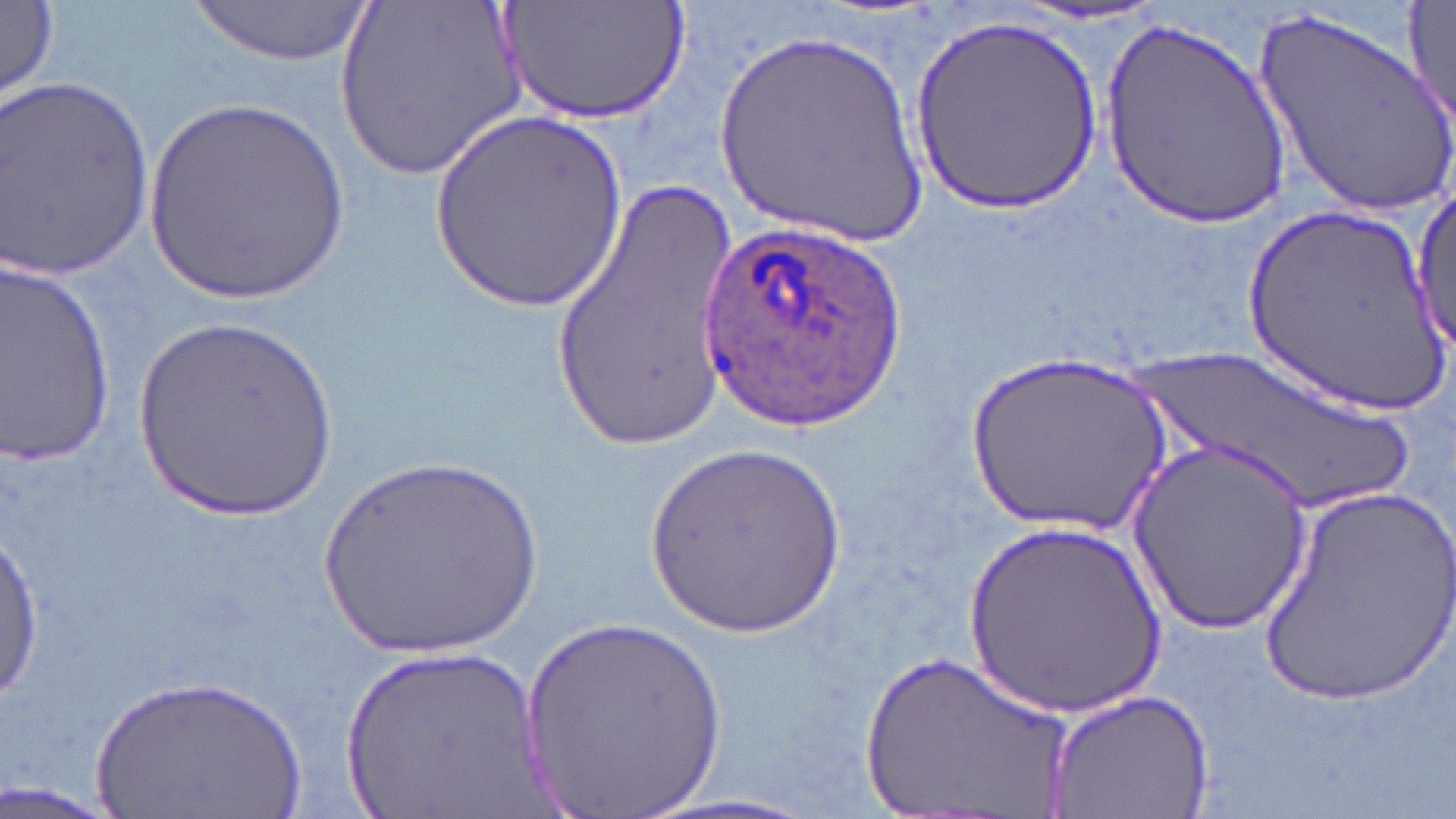

slide_level_diagnosis: Plasmodium ovale
preparation: thin blood smear
plasmodium_ovale_infected_red_blood_cell_locations: 'approximate bounding boxes as (x1, y1, x2, y2) in pixels: (694, 220, 902, 426)'
image_size: 1456×819 pixels
uninfected_red_blood_cell_locations: 'approximate bounding boxes as (x1, y1, x2, y2) in pixels: (333, 0, 529, 181), (497, 0, 694, 124), (1402, 0, 1456, 130), (1, 2, 61, 104), (190, 2, 374, 69), (1000, 4, 1177, 28), (1249, 6, 1456, 216), (911, 16, 1103, 214), (1098, 21, 1294, 227), (711, 26, 929, 252), (2, 74, 157, 278), (142, 98, 352, 310), (430, 110, 627, 317), (551, 170, 748, 450), (1412, 190, 1455, 354), (1236, 204, 1452, 414), (0, 263, 118, 464), (132, 320, 339, 527), (1129, 343, 1422, 513), (966, 346, 1176, 538), (1129, 439, 1314, 635), (646, 443, 848, 644), (310, 448, 553, 665), (1255, 481, 1456, 706), (962, 515, 1175, 719), (0, 519, 47, 709), (517, 611, 735, 819), (338, 643, 552, 819), (857, 644, 1079, 819), (89, 674, 311, 819), (1046, 687, 1214, 818), (0, 780, 121, 819)'
stain: May-Grünwald-Giemsa
field_of_view: single
modality: light microscopy
magnification: 1000x